State which parasite is depicted.
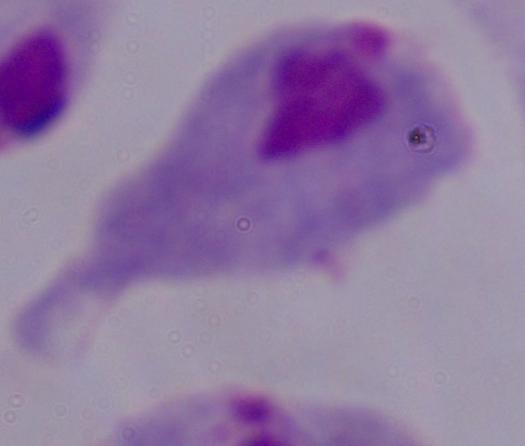

This is a trichomonad.

Micrograph. Captured at 1000x magnification.